Name the parasite shown.
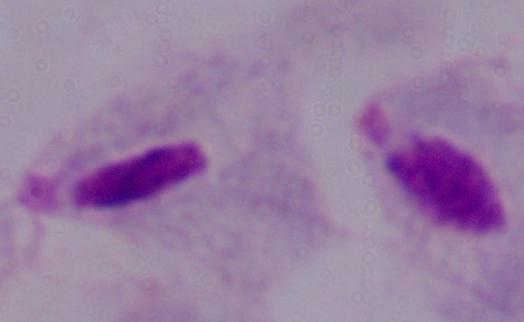
This is a trichomonad.

Summary:
  - Modality: micrograph
  - Magnification: 1000x